Classify this cell by malaria status.
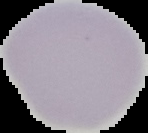

It is uninfected.

Summary:
  - Image size: 148×133 pixels
  - Preparation: thin blood film
  - Image type: segmented cell region with the area outside set to black